Classify this cell by malaria status.
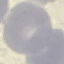
It is uninfected.

Thin smear of blood. Giemsa stain. Photographed with a smartphone camera at the microscope eyepiece. Cell patch, automatically extracted from a larger field of view and resized to 64 × 64 pixels.